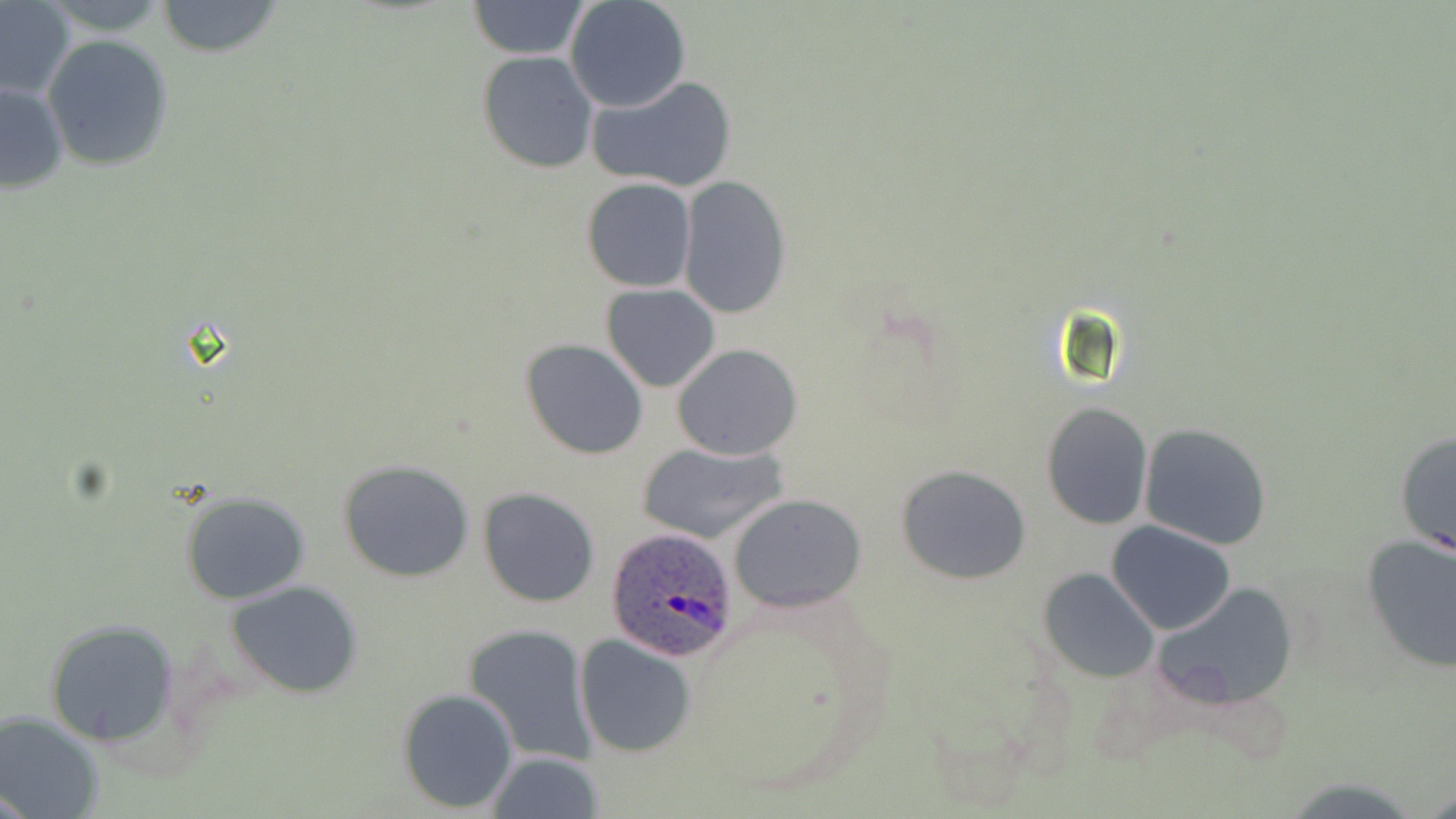
Summary:
  - Coordinate format: approximate bounding boxes as (x1,y1)-(x2,y2) corner pairs in pixels
  - Plasmodium ovale-infected red blood cell locations: (604,529)-(741,662)
  - Uninfected red blood cell locations: (40,0)-(172,33), (466,0)-(592,59), (155,1)-(284,57), (565,1)-(691,113), (0,3)-(75,100), (41,34)-(175,172), (476,50)-(598,173), (587,75)-(739,194), (0,81)-(70,194), (678,176)-(792,319), (581,179)-(698,293), (601,283)-(720,392), (520,339)-(649,459), (672,344)-(803,461), (1041,401)-(1153,531), (1140,423)-(1273,550), (1393,430)-(1456,558), (638,442)-(789,545), (336,459)-(477,584), (897,463)-(1033,585), (477,487)-(600,608), (178,491)-(312,604), (727,492)-(867,613), (1107,522)-(1236,635), (1359,533)-(1455,673), (1039,566)-(1161,682), (225,581)-(366,699), (1151,581)-(1299,705), (43,619)-(182,746), (464,624)-(597,765), (575,635)-(695,756), (397,687)-(520,813), (1,712)-(103,817), (485,752)-(605,819)
  - Slide-level diagnosis: Plasmodium ovale
  - Field of view: one of a larger specimen
  - Image size: 1456×819 pixels
  - Magnification: 1000x
  - Stain: May-Grünwald-Giemsa
  - Preparation: thin blood smear
  - Modality: light microscopy